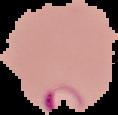
Segmented cell region on a black background. From a thin blood film. Malaria status: parasitized. Image is 118×115 pixels.